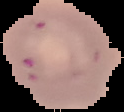
{
  "result": "no Plasmodium parasites seen",
  "image_size": "124×112 pixels",
  "preparation": "thin blood film",
  "image_type": "segmented cell region with the area outside set to black"
}